Assess the morphology of the erythrocytes.
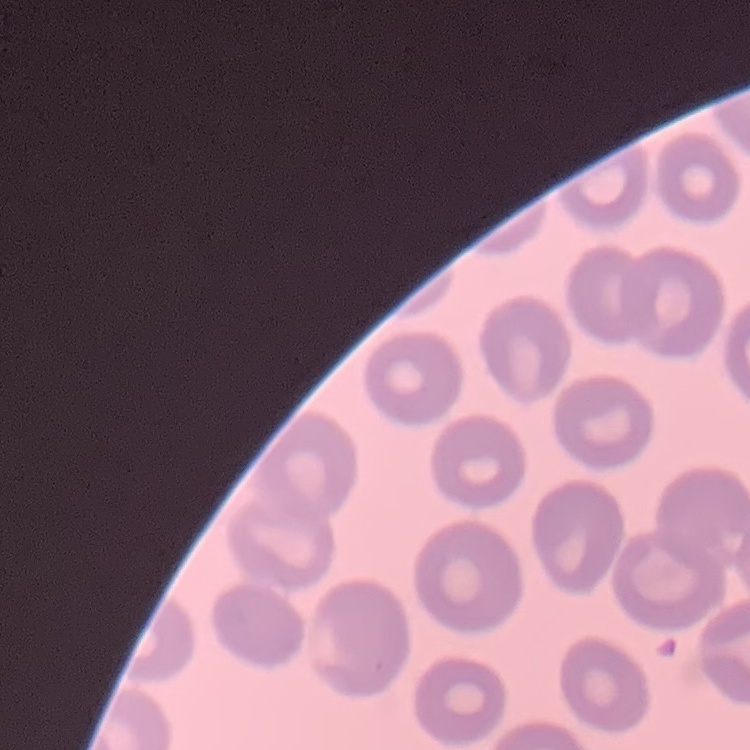

No rouleaux formation.

image type = square crop of a larger photomicrograph
preparation = thin blood smear
stain = Field's or Giemsa